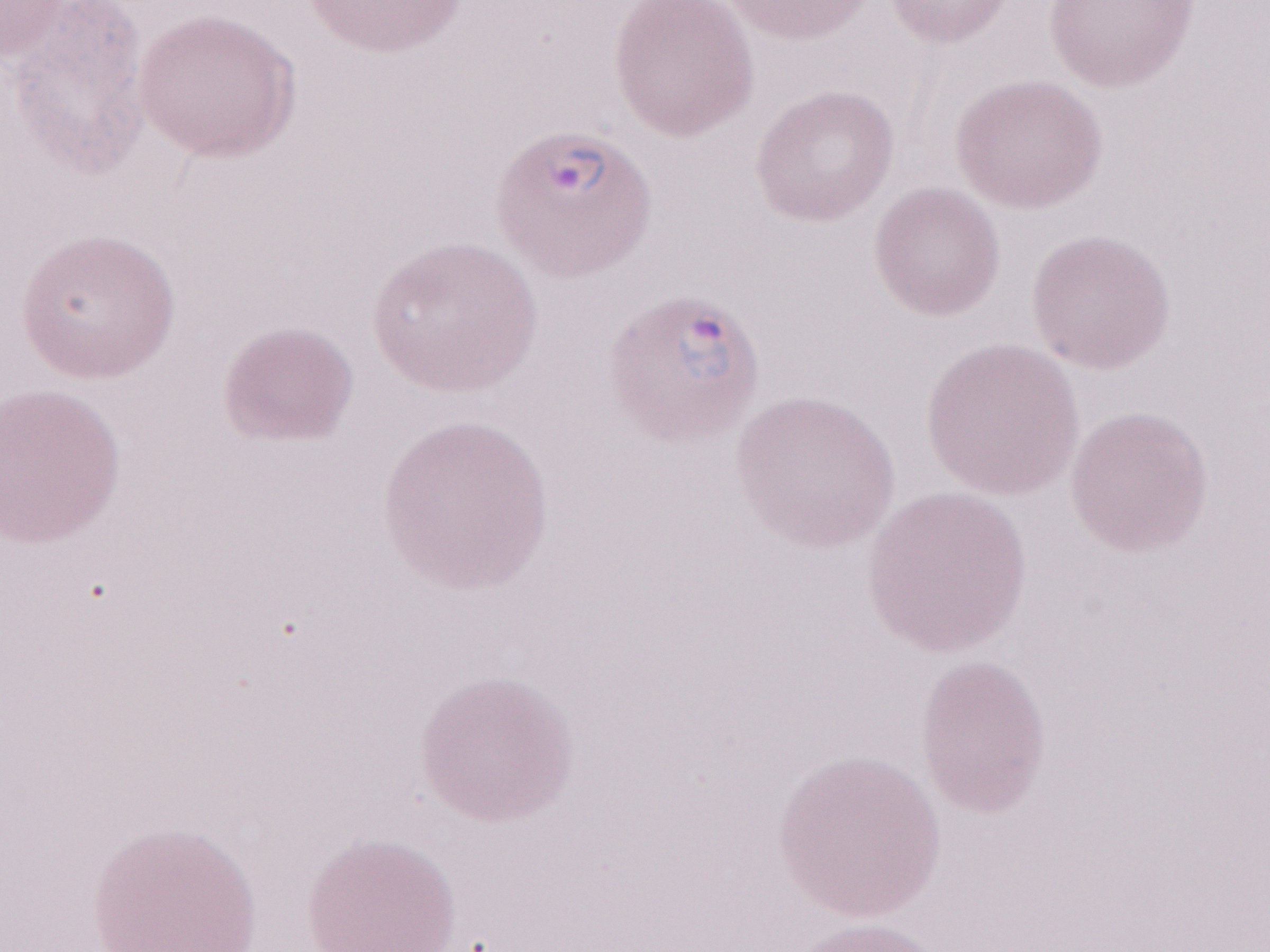 May-Grünwald-Giemsa stain. 1,000x magnification. Image is 1270×952 pixels. One field of this slide. Patient-level malaria diagnosis: positive. Olympus BX43 microscope, Olympus DP73 camera. Thin blood smear.